Report the malaria status of this cell.
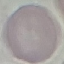

It is uninfected.

Acquired by smartphone through the microscope eyepiece. Cell patch, automatically extracted from a larger field of view and resized to 64 × 64 pixels. Thin blood smear. Giemsa stain.